Identify the parasite.
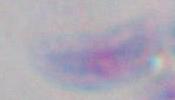

Toxoplasma gondii.

modality = photomicrograph
magnification = 1000x